Identify the blood parasite species.
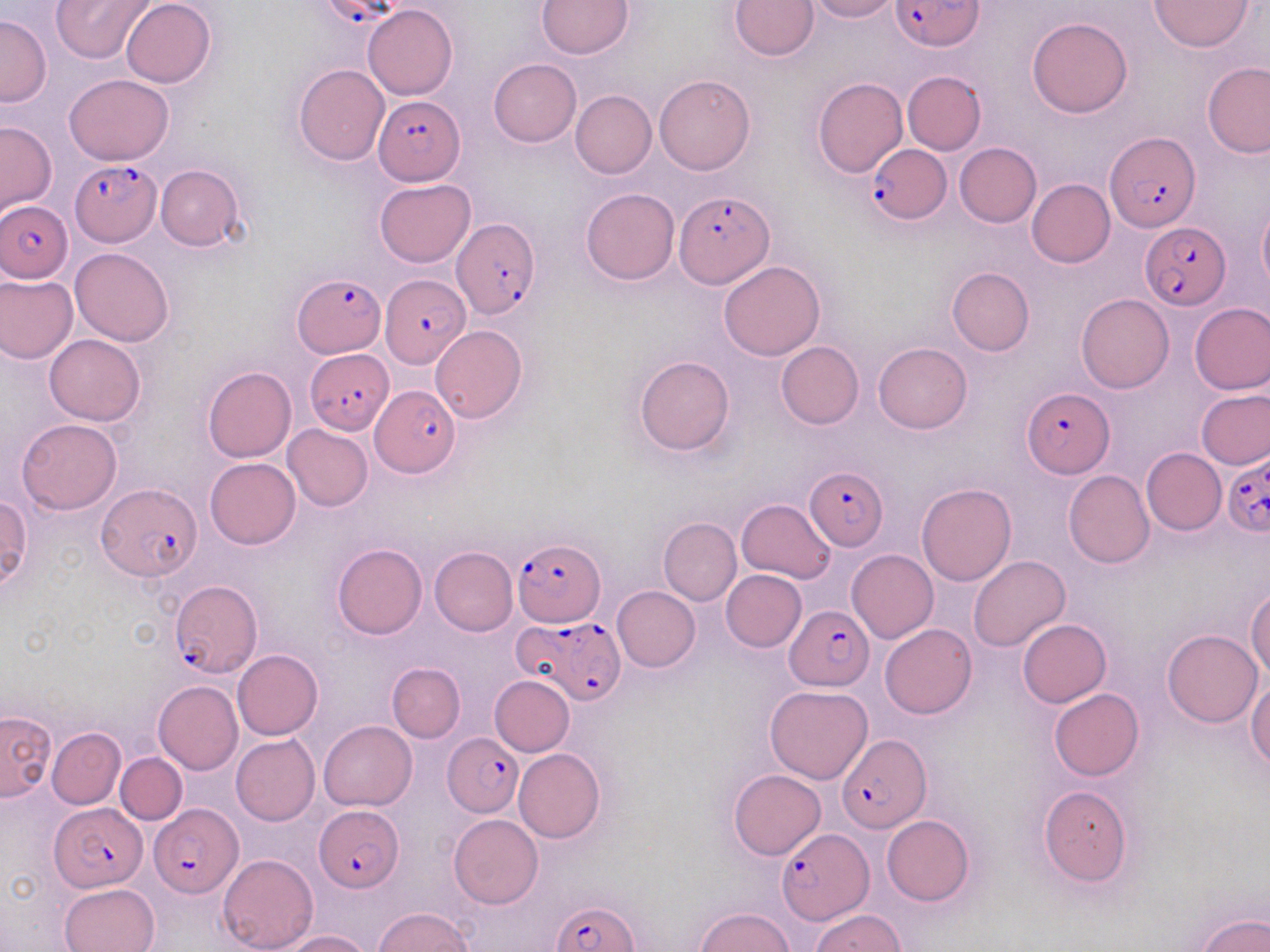

Plasmodium falciparum.

Summary:
  - Coordinate format: approximate bounding boxes as (x1, y1, x2, y2) in pixels
  - Plasmodium falciparum-infected red blood cell locations: (893, 0, 982, 50), (373, 95, 464, 185), (1105, 132, 1200, 231), (866, 142, 949, 224), (70, 160, 162, 247), (674, 191, 774, 287), (1, 200, 73, 282), (451, 217, 540, 320), (1141, 222, 1230, 310), (294, 272, 384, 356), (380, 275, 467, 367), (304, 347, 394, 434), (371, 384, 459, 479), (1022, 386, 1114, 478), (1221, 449, 1270, 538), (807, 465, 890, 552), (98, 484, 200, 582), (513, 534, 604, 629), (169, 581, 262, 677), (785, 605, 874, 692), (516, 615, 626, 705), (444, 732, 523, 814), (838, 734, 931, 834), (50, 804, 145, 892), (150, 804, 241, 898), (315, 804, 404, 890), (777, 829, 871, 925), (551, 900, 638, 952)
  - Uninfected red blood cell locations: (50, 0, 154, 64), (537, 0, 634, 58), (730, 0, 818, 60), (805, 0, 897, 22), (1150, 0, 1253, 51), (120, 1, 216, 87), (363, 4, 457, 99), (0, 14, 51, 107), (1026, 16, 1134, 119), (489, 58, 582, 148), (1202, 61, 1270, 156), (294, 64, 391, 166), (901, 70, 986, 154), (63, 73, 173, 164), (654, 74, 755, 175), (813, 77, 908, 179), (571, 90, 657, 178), (0, 121, 57, 216), (953, 143, 1041, 227), (155, 163, 245, 251), (1027, 178, 1115, 267), (375, 179, 475, 266), (581, 187, 680, 285), (1257, 203, 1270, 294), (70, 248, 174, 346), (719, 261, 825, 360), (946, 267, 1034, 356), (0, 274, 77, 363), (1075, 294, 1173, 394), (1189, 303, 1270, 394), (431, 326, 527, 424), (44, 333, 147, 424), (776, 341, 864, 429), (873, 342, 972, 434), (634, 356, 734, 456), (203, 366, 297, 463), (1197, 390, 1270, 470), (17, 418, 123, 514), (283, 424, 373, 511), (1141, 448, 1225, 535), (205, 458, 300, 549), (1064, 471, 1155, 568), (915, 484, 1016, 586), (1, 494, 32, 589), (738, 500, 837, 583), (658, 518, 741, 605), (332, 543, 426, 639), (430, 546, 518, 636), (847, 550, 938, 644), (968, 554, 1071, 652), (721, 569, 807, 652), (612, 586, 700, 672), (1246, 587, 1269, 682), (1017, 619, 1112, 707), (880, 624, 976, 719), (1162, 629, 1262, 727), (232, 649, 322, 739), (386, 663, 465, 742), (489, 675, 575, 755), (1247, 678, 1270, 771), (153, 680, 242, 774), (766, 686, 873, 783), (1048, 689, 1144, 780), (0, 712, 56, 800), (318, 721, 417, 811), (47, 727, 125, 809), (231, 734, 319, 826), (513, 748, 604, 844), (116, 753, 187, 824), (727, 769, 825, 860), (1038, 786, 1133, 886), (448, 814, 544, 908), (882, 815, 974, 906), (218, 853, 318, 952), (60, 883, 159, 952), (374, 907, 476, 952), (694, 907, 794, 952), (811, 909, 905, 951), (1193, 911, 1270, 952), (278, 930, 373, 952)
  - Stain: May-Grünwald-Giemsa
  - Image size: 1270×952 pixels
  - Magnification: 1000x
  - Field of view: one of a larger specimen
  - Preparation: thin blood smear
  - Modality: optical microscopy